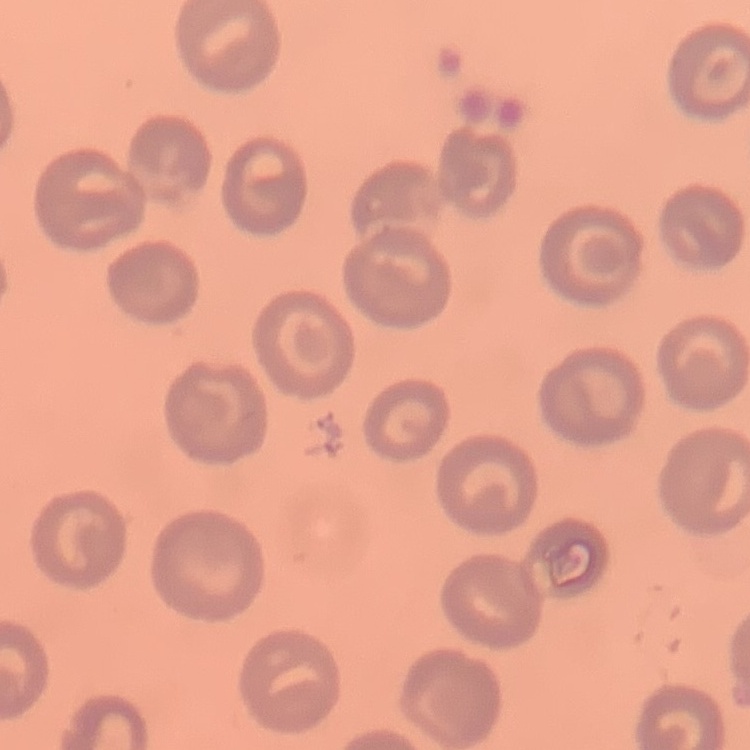

{
  "red_blood_cell_morphology": "no rouleaux formation",
  "image_type": "one tile cut from a larger photomicrograph",
  "preparation": "thin peripheral smear",
  "stain": "Field's or Giemsa"
}